Point out each malaria parasite.
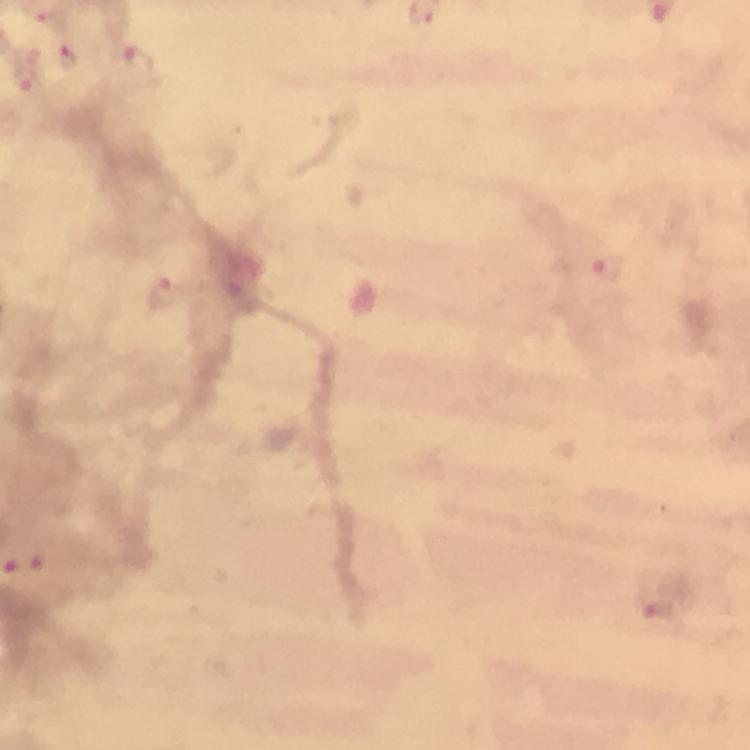

Approximate centers as [x, y] in pixels.
Malaria parasites: [49, 20], [68, 58], [136, 63], [25, 81], [606, 268], [166, 294], [35, 562], [653, 607].

Immersion oil was used. Smartphone photograph taken through a microscope. Image is 750×750 pixels. Thick blood film. 100x magnification. From a diagnostic examination for malaria. Cropped region of a single field of view. Giemsa stain.